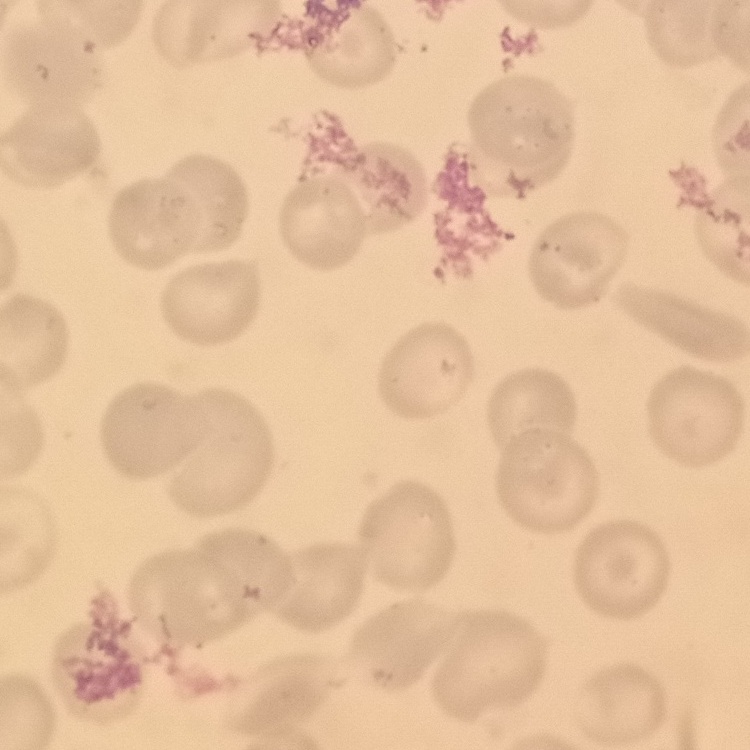 The erythrocytes exhibit no rouleaux formation. One tile cut from a larger photomicrograph. Thin blood smear. Field's or Giemsa stain.